Name the blood parasite species.
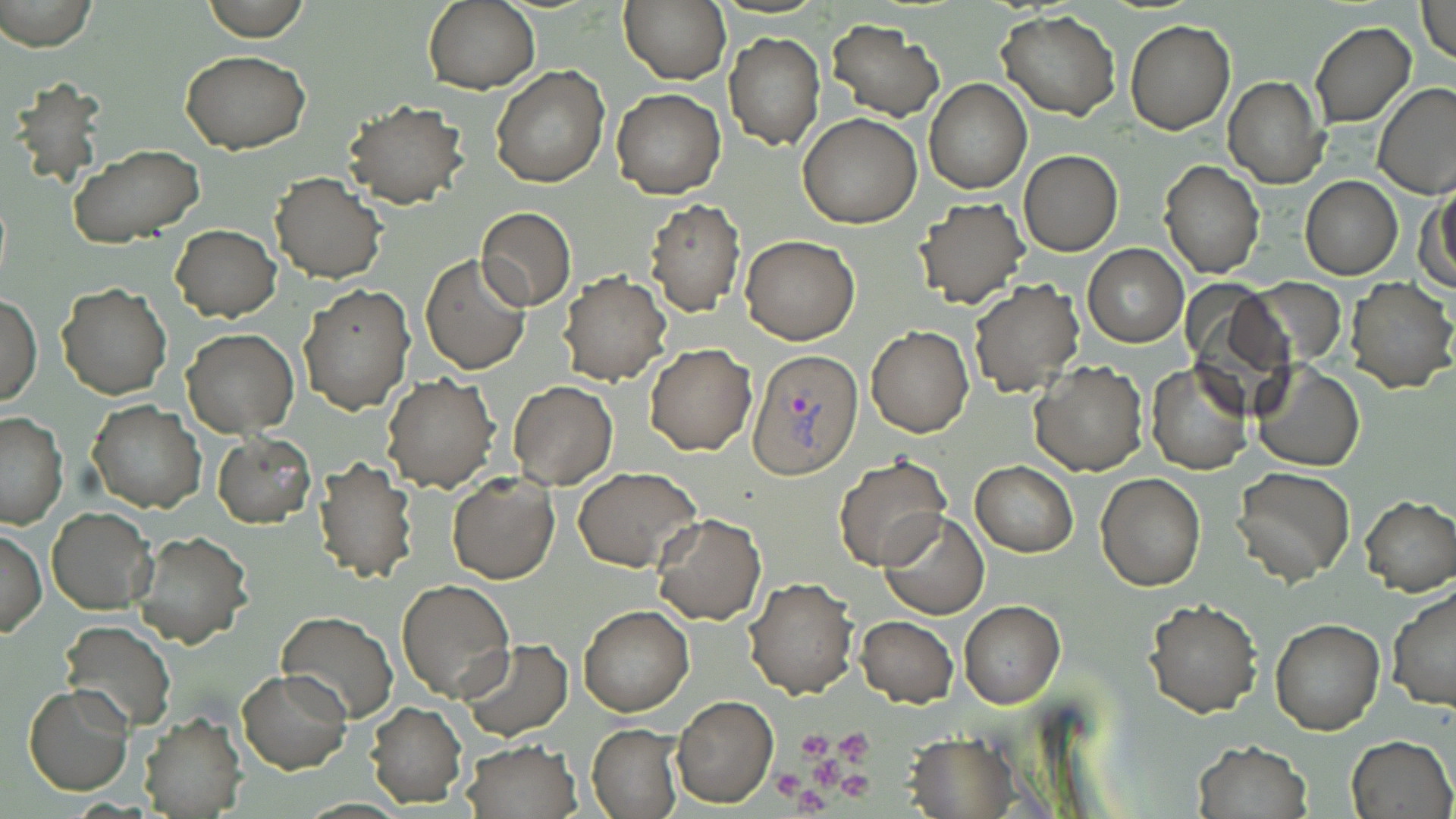
Plasmodium vivax.

Summary:
  - Coordinate format: approximate bounding boxes as named x1/y1/x2/y2 corners in pixels
  - Plasmodium vivax-infected red blood cell locations: (x1=748, y1=347, x2=865, y2=479)
  - Platelet locations: (x1=798, y1=730, x2=832, y2=758), (x1=835, y1=730, x2=873, y2=761), (x1=811, y1=759, x2=841, y2=787), (x1=773, y1=768, x2=804, y2=798), (x1=841, y1=771, x2=872, y2=800), (x1=794, y1=786, x2=827, y2=815)
  - Uninfected red blood cell locations: (x1=1, y1=0, x2=99, y2=51), (x1=203, y1=0, x2=309, y2=41), (x1=423, y1=1, x2=541, y2=94), (x1=619, y1=1, x2=730, y2=84), (x1=1417, y1=1, x2=1456, y2=64), (x1=996, y1=10, x2=1120, y2=121), (x1=826, y1=19, x2=945, y2=120), (x1=1125, y1=20, x2=1234, y2=134), (x1=1309, y1=22, x2=1417, y2=128), (x1=724, y1=31, x2=825, y2=149), (x1=182, y1=51, x2=311, y2=153), (x1=491, y1=65, x2=608, y2=187), (x1=1223, y1=75, x2=1328, y2=189), (x1=924, y1=79, x2=1032, y2=194), (x1=1372, y1=83, x2=1456, y2=199), (x1=612, y1=89, x2=725, y2=200), (x1=343, y1=101, x2=469, y2=208), (x1=797, y1=112, x2=922, y2=229), (x1=68, y1=144, x2=205, y2=246), (x1=1019, y1=151, x2=1122, y2=255), (x1=1159, y1=159, x2=1264, y2=279), (x1=269, y1=171, x2=386, y2=284), (x1=1300, y1=175, x2=1403, y2=280), (x1=1422, y1=181, x2=1456, y2=293), (x1=915, y1=197, x2=1030, y2=309), (x1=644, y1=199, x2=746, y2=317), (x1=476, y1=207, x2=577, y2=311), (x1=170, y1=224, x2=280, y2=321), (x1=740, y1=236, x2=860, y2=345), (x1=1081, y1=244, x2=1189, y2=347), (x1=419, y1=253, x2=531, y2=375), (x1=557, y1=274, x2=671, y2=387), (x1=1248, y1=277, x2=1346, y2=364), (x1=1344, y1=278, x2=1456, y2=393), (x1=969, y1=279, x2=1085, y2=398), (x1=1180, y1=282, x2=1297, y2=410), (x1=299, y1=283, x2=413, y2=413), (x1=58, y1=285, x2=172, y2=400), (x1=2, y1=292, x2=41, y2=408), (x1=866, y1=325, x2=974, y2=437), (x1=182, y1=329, x2=299, y2=438), (x1=646, y1=344, x2=755, y2=456), (x1=1030, y1=362, x2=1146, y2=476), (x1=1251, y1=362, x2=1364, y2=471), (x1=1145, y1=363, x2=1250, y2=476), (x1=383, y1=373, x2=499, y2=492), (x1=507, y1=380, x2=618, y2=489), (x1=87, y1=402, x2=205, y2=513), (x1=0, y1=412, x2=68, y2=529), (x1=212, y1=433, x2=315, y2=528), (x1=311, y1=455, x2=417, y2=584), (x1=832, y1=455, x2=953, y2=571), (x1=971, y1=461, x2=1077, y2=557), (x1=1233, y1=466, x2=1355, y2=584), (x1=573, y1=467, x2=702, y2=571), (x1=447, y1=471, x2=559, y2=584), (x1=1096, y1=473, x2=1205, y2=591), (x1=1360, y1=495, x2=1456, y2=596), (x1=47, y1=508, x2=158, y2=614), (x1=880, y1=512, x2=990, y2=620), (x1=650, y1=513, x2=767, y2=625), (x1=1, y1=528, x2=46, y2=636), (x1=130, y1=528, x2=254, y2=647), (x1=745, y1=575, x2=858, y2=699), (x1=395, y1=578, x2=517, y2=703), (x1=1387, y1=585, x2=1456, y2=714), (x1=1144, y1=599, x2=1262, y2=717), (x1=959, y1=601, x2=1066, y2=708), (x1=578, y1=606, x2=694, y2=717), (x1=278, y1=610, x2=398, y2=724), (x1=856, y1=615, x2=959, y2=708), (x1=1269, y1=617, x2=1385, y2=735), (x1=59, y1=619, x2=176, y2=733), (x1=461, y1=637, x2=573, y2=741), (x1=237, y1=669, x2=351, y2=774), (x1=25, y1=684, x2=134, y2=797), (x1=672, y1=695, x2=778, y2=809), (x1=365, y1=702, x2=468, y2=808), (x1=138, y1=709, x2=247, y2=818), (x1=588, y1=723, x2=684, y2=819), (x1=904, y1=733, x2=1018, y2=818), (x1=1347, y1=733, x2=1455, y2=819), (x1=459, y1=740, x2=582, y2=819), (x1=1193, y1=740, x2=1311, y2=819)
  - Field of view: single
  - Stain: May-Grünwald-Giemsa
  - Modality: light microscopy
  - Magnification: 1000x
  - Image size: 1456×819 pixels
  - Preparation: thin blood smear